Outline each Plasmodium vivax-infected red blood cell.
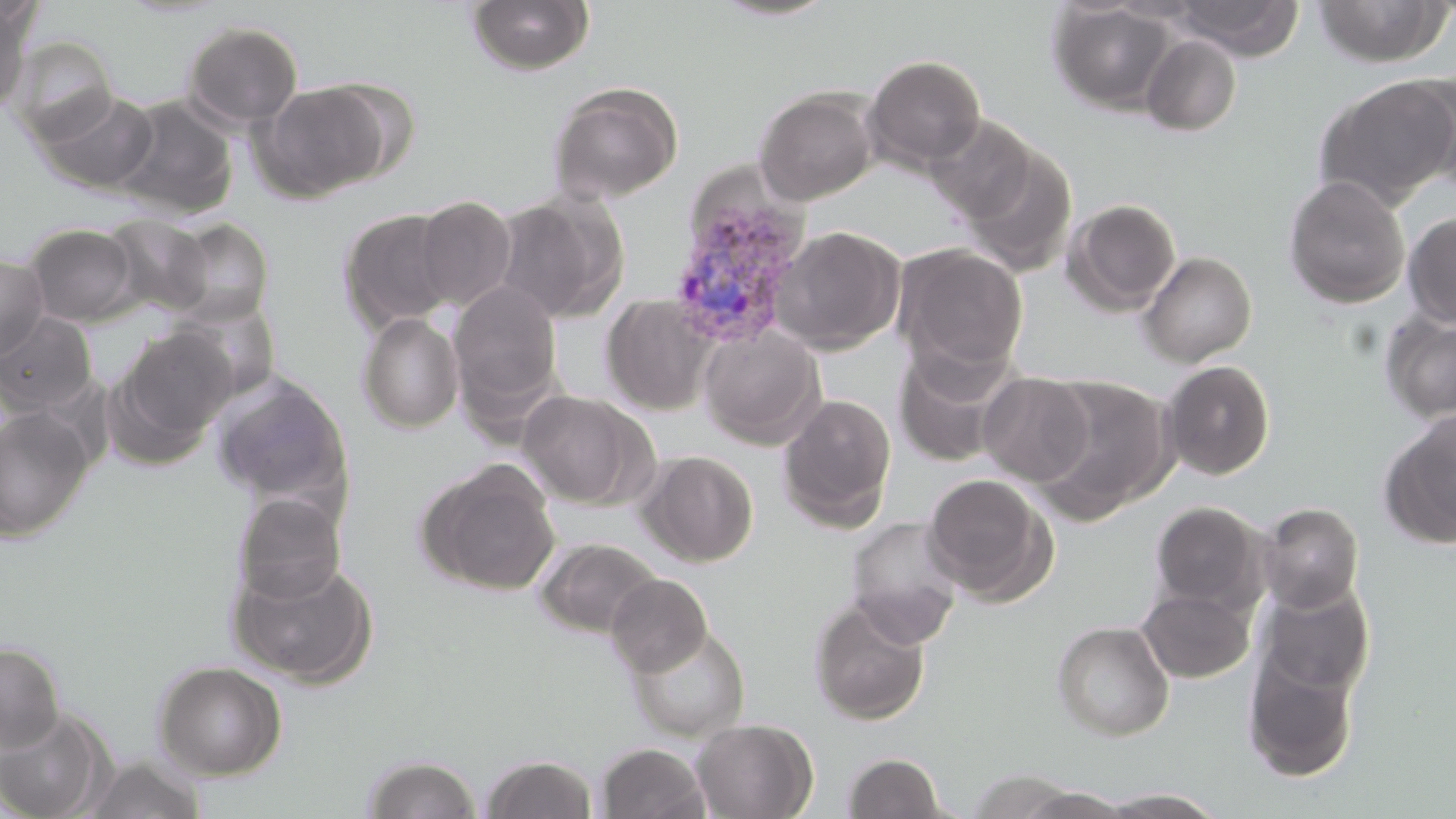
Approximate bounding boxes as (x1, y1, x2, y2) in pixels.
Plasmodium vivax-infected red blood cells: (666, 182, 812, 350).

Uninfected red blood cell locations: (1169, 0, 1304, 59), (1312, 0, 1452, 68), (466, 1, 596, 75), (706, 1, 841, 22), (1048, 1, 1177, 115), (0, 4, 34, 115), (182, 21, 303, 129), (1140, 34, 1242, 136), (6, 35, 119, 145), (864, 54, 986, 170), (1404, 69, 1456, 195), (1313, 74, 1456, 209), (548, 80, 684, 203), (252, 82, 391, 202), (753, 86, 879, 206), (38, 90, 159, 194), (112, 95, 238, 221), (925, 115, 1040, 223), (959, 145, 1078, 277), (1281, 175, 1411, 309), (492, 191, 627, 323), (415, 195, 517, 311), (1063, 198, 1181, 315), (338, 208, 459, 332), (1402, 212, 1456, 328), (101, 214, 213, 317), (166, 218, 274, 325), (24, 222, 140, 325), (770, 225, 905, 354), (893, 243, 1027, 375), (1138, 251, 1257, 366), (0, 252, 50, 362), (448, 282, 563, 410), (602, 294, 718, 415), (167, 298, 281, 400), (1378, 310, 1456, 422), (357, 312, 465, 433), (0, 313, 97, 415), (698, 324, 825, 449), (113, 325, 237, 448), (893, 344, 1020, 467), (1160, 360, 1276, 480), (978, 371, 1095, 486), (210, 373, 352, 508), (1032, 375, 1174, 518), (518, 389, 652, 509), (777, 393, 897, 531), (0, 406, 95, 543), (1381, 411, 1456, 548), (638, 450, 759, 567), (418, 459, 561, 595), (921, 473, 1056, 603), (233, 493, 347, 604), (1151, 501, 1267, 613), (1257, 502, 1365, 613), (845, 516, 965, 645), (535, 538, 661, 639), (228, 555, 379, 688), (606, 573, 712, 676), (1257, 580, 1374, 697), (1136, 587, 1254, 682), (809, 598, 931, 725), (1051, 620, 1174, 740), (625, 624, 751, 742), (0, 641, 65, 754), (1242, 647, 1360, 782), (152, 660, 287, 780), (0, 705, 116, 819), (691, 718, 817, 818), (596, 742, 711, 819), (842, 752, 948, 818), (361, 754, 483, 818), (481, 754, 599, 818), (82, 756, 206, 819), (965, 769, 1086, 818), (1012, 787, 1137, 819), (1098, 789, 1226, 818). Slide-level diagnosis: Plasmodium vivax. Image is 1456×819 pixels. Captured at 1000x magnification. Thin blood smear. May-Grünwald-Giemsa-stained preparation. One field of a larger specimen. Optical microscopy.